Assess this cell for malaria.
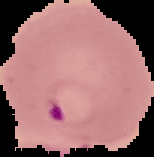
It is parasitized.

preparation = thin blood film
image type = segmented cell region on a black background
image size = 154×157 pixels